Name the parasite shown.
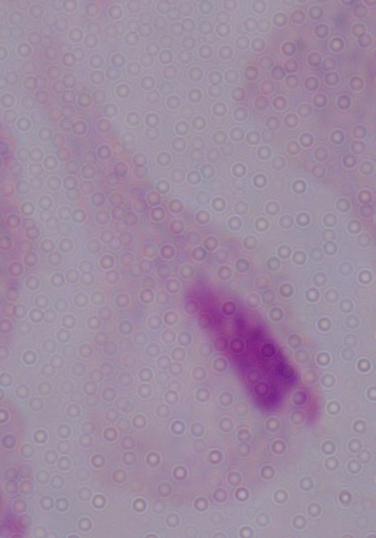

This is a trichomonad.

Photomicrograph. Captured at 1000x magnification.